Report the malaria status of this cell.
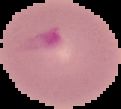

It is parasitized.

preparation: thin blood film
image_type: cell region segmented out of the field of view; surrounding area masked to black
image_size: 121×109 pixels